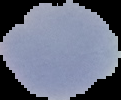

image_size: 121×100 pixels
result: malaria parasites detected
preparation: thin blood film
image_type: segmented cell region with the area outside set to black